Find each white blood cell.
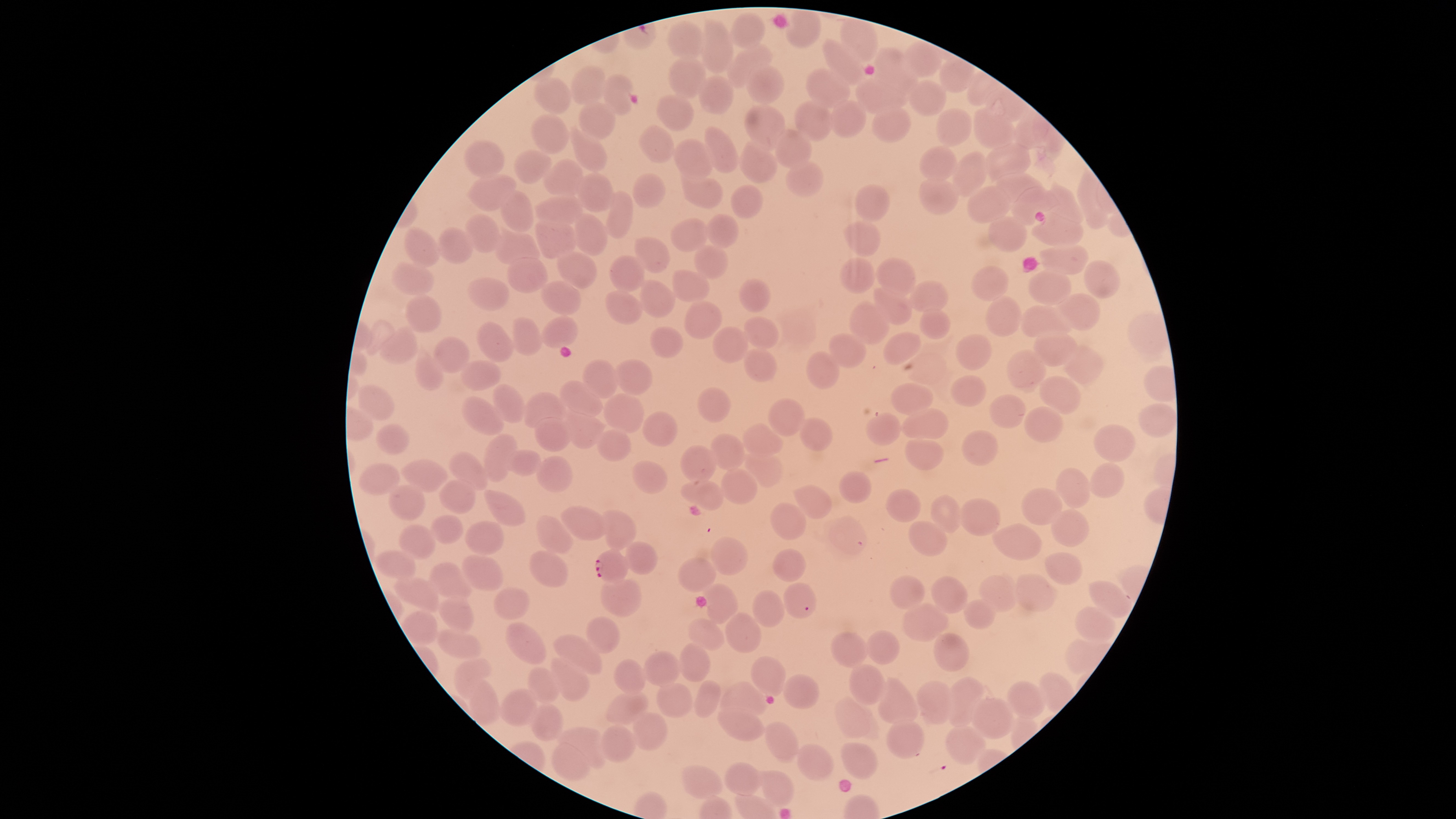
No white blood cells identified.

Approximate bounding boxes as {left, top, right, bottom} in pixels. Uninfected red blood cells: {732, 13, 765, 48}, {702, 19, 734, 73}, {668, 22, 705, 60}, {823, 40, 866, 87}, {726, 43, 774, 87}, {874, 47, 906, 79}, {668, 57, 705, 100}, {873, 60, 919, 97}, {746, 64, 784, 104}, {570, 66, 606, 104}, {805, 68, 851, 109}, {603, 74, 633, 117}, {698, 76, 733, 115}, {855, 76, 908, 115}, {534, 77, 570, 113}, {908, 80, 947, 115}, {656, 94, 693, 132}, {831, 100, 866, 138}, {794, 101, 832, 141}, {578, 102, 616, 141}, {745, 104, 785, 152}, {871, 107, 910, 143}, {970, 107, 1015, 149}, {936, 108, 972, 148}, {531, 114, 569, 154}, {572, 125, 606, 172}, {638, 125, 675, 163}, {704, 126, 739, 173}, {774, 129, 811, 170}, {673, 139, 713, 181}, {463, 140, 505, 178}, {740, 140, 778, 184}, {984, 141, 1031, 182}, {919, 146, 959, 184}, {514, 150, 551, 184}, {952, 152, 988, 197}, {542, 158, 583, 196}, {786, 162, 824, 198}, {469, 172, 516, 211}, {632, 172, 666, 208}, {991, 172, 1042, 203}, {576, 173, 616, 213}, {681, 177, 723, 209}, {919, 177, 959, 215}, {1045, 184, 1084, 226}, {856, 185, 889, 221}, {967, 185, 1010, 223}, {730, 186, 763, 219}, {1011, 187, 1057, 226}, {499, 189, 533, 232}, {607, 191, 631, 239}, {534, 197, 582, 227}, {1031, 211, 1083, 248}, {567, 212, 607, 257}, {705, 213, 739, 248}, {464, 214, 500, 253}, {535, 215, 575, 260}, {988, 215, 1028, 253}, {670, 218, 709, 252}, {844, 220, 881, 257}, {404, 228, 441, 268}, {437, 228, 474, 264}, {492, 231, 542, 263}, {633, 237, 671, 273}, {1040, 245, 1088, 275}, {693, 246, 728, 280}, {556, 248, 597, 289}, {610, 254, 645, 293}, {507, 258, 548, 293}, {839, 258, 875, 293}, {876, 258, 916, 297}, {1084, 260, 1121, 299}, {394, 261, 434, 295}, {972, 265, 1009, 303}, {1028, 269, 1071, 305}, {672, 270, 711, 302}, {465, 275, 509, 309}, {739, 277, 770, 312}, {638, 280, 675, 318}, {540, 281, 582, 315}, {909, 281, 950, 312}, {874, 284, 913, 325}, {604, 290, 644, 325}, {1057, 293, 1100, 331}, {404, 295, 441, 334}, {985, 295, 1022, 337}, {686, 301, 722, 339}, {850, 303, 889, 345}, {1020, 305, 1073, 337}, {920, 309, 951, 339}, {745, 315, 780, 350}, {512, 317, 543, 355}, {542, 317, 577, 347}, {365, 319, 396, 356}, {476, 320, 513, 362}, {713, 325, 748, 363}, {650, 326, 683, 357}, {379, 327, 420, 364}, {1033, 331, 1079, 368}, {884, 332, 922, 365}, {829, 333, 866, 369}, {955, 333, 993, 371}, {433, 338, 470, 374}, {1060, 344, 1103, 383}, {744, 347, 776, 381}, {1006, 349, 1046, 391}, {806, 351, 839, 389}, {415, 354, 444, 391}, {582, 359, 619, 400}, {460, 360, 500, 390}, {614, 360, 653, 395}, {951, 374, 987, 407}, {1039, 376, 1081, 414}, {559, 381, 604, 417}, {890, 382, 933, 416}, {493, 383, 526, 421}, {358, 385, 394, 421}, {697, 387, 731, 423}, {525, 392, 565, 431}, {602, 393, 645, 433}, {989, 394, 1026, 428}, {462, 395, 504, 436}, {770, 399, 806, 437}, {1138, 403, 1178, 437}, {1023, 406, 1063, 443}, {901, 408, 948, 440}, {564, 410, 604, 448}, {642, 412, 677, 446}, {866, 413, 900, 445}, {534, 417, 571, 452}, {799, 417, 832, 451}, {741, 421, 783, 458}, {376, 424, 410, 455}, {1093, 425, 1136, 463}, {596, 429, 631, 461}, {961, 430, 999, 466}, {483, 433, 516, 481}, {710, 433, 747, 469}, {904, 435, 945, 470}, {680, 445, 717, 481}, {742, 449, 783, 491}, {503, 450, 541, 475}, {448, 451, 489, 491}, {535, 456, 572, 492}, {402, 460, 448, 493}, {631, 460, 667, 492}, {359, 463, 400, 496}, {1090, 463, 1125, 499}, {721, 465, 757, 504}, {1055, 467, 1090, 509}, {840, 470, 872, 503}, {682, 478, 723, 510}, {438, 480, 476, 514}, {388, 483, 425, 522}, {794, 484, 831, 518}, {885, 488, 921, 522}, {1020, 488, 1063, 526}, {484, 490, 527, 528}, {930, 494, 962, 534}, {959, 499, 1001, 535}, {770, 502, 806, 539}, {559, 506, 609, 540}, {601, 508, 635, 549}, {1051, 509, 1088, 547}, {535, 514, 577, 554}, {430, 515, 463, 544}, {464, 520, 503, 555}, {908, 520, 947, 559}, {991, 523, 1041, 560}, {399, 525, 435, 560}, {711, 536, 747, 575}, {624, 540, 656, 574}, {772, 549, 805, 582}, {375, 550, 416, 581}, {528, 550, 567, 585}, {1043, 551, 1084, 587}, {461, 555, 504, 591}, {678, 557, 717, 592}, {428, 563, 473, 601}, {1013, 573, 1056, 613}, {601, 575, 642, 617}, {932, 575, 968, 613}, {979, 575, 1017, 613}, {394, 576, 441, 611}, {889, 576, 924, 611}, {1089, 581, 1130, 618}, {784, 582, 816, 618}, {705, 584, 739, 623}, {493, 587, 530, 620}, {753, 590, 785, 627}, {438, 595, 474, 634}, {965, 601, 996, 629}, {903, 604, 950, 643}, {1074, 607, 1116, 643}, {725, 612, 761, 652}, {585, 617, 620, 654}, {689, 617, 724, 650}, {504, 623, 547, 665}, {437, 630, 482, 660}, {867, 630, 899, 665}, {830, 632, 868, 668}, {934, 633, 970, 673}, {553, 634, 603, 676}, {679, 643, 708, 683}, {643, 650, 681, 686}, {751, 656, 785, 697}, {454, 658, 493, 700}, {551, 658, 590, 702}, {613, 659, 647, 694}, {849, 664, 885, 706}, {528, 667, 561, 703}, {784, 674, 820, 709}, {945, 676, 983, 727}, {878, 678, 917, 725}, {469, 679, 501, 725}, {695, 680, 721, 718}, {720, 680, 768, 720}, {1008, 680, 1044, 719}, {917, 681, 952, 725}, {657, 683, 693, 720}, {498, 690, 537, 726}, {606, 691, 649, 724}, {835, 696, 872, 739}, {971, 698, 1014, 740}, {528, 705, 564, 740}, {717, 709, 765, 742}, {632, 711, 666, 751}, {765, 720, 798, 763}, {887, 720, 924, 759}, {599, 725, 636, 763}, {944, 725, 986, 765}, {557, 728, 610, 768}, {841, 742, 878, 780}, {552, 743, 589, 780}, {798, 744, 833, 780}, {724, 762, 763, 797}, {681, 765, 722, 799}, {762, 771, 794, 808}. Parasitized red blood cells: {595, 549, 628, 584}. Giemsa-stained preparation. The visible region is circular. Photographed with a smartphone camera through the microscope eyepiece. Species: Plasmodium falciparum. Image is 1456×819 pixels. One field of view of the specimen. Thin blood film. Presence: malaria parasites seen.